Assess for malaria.
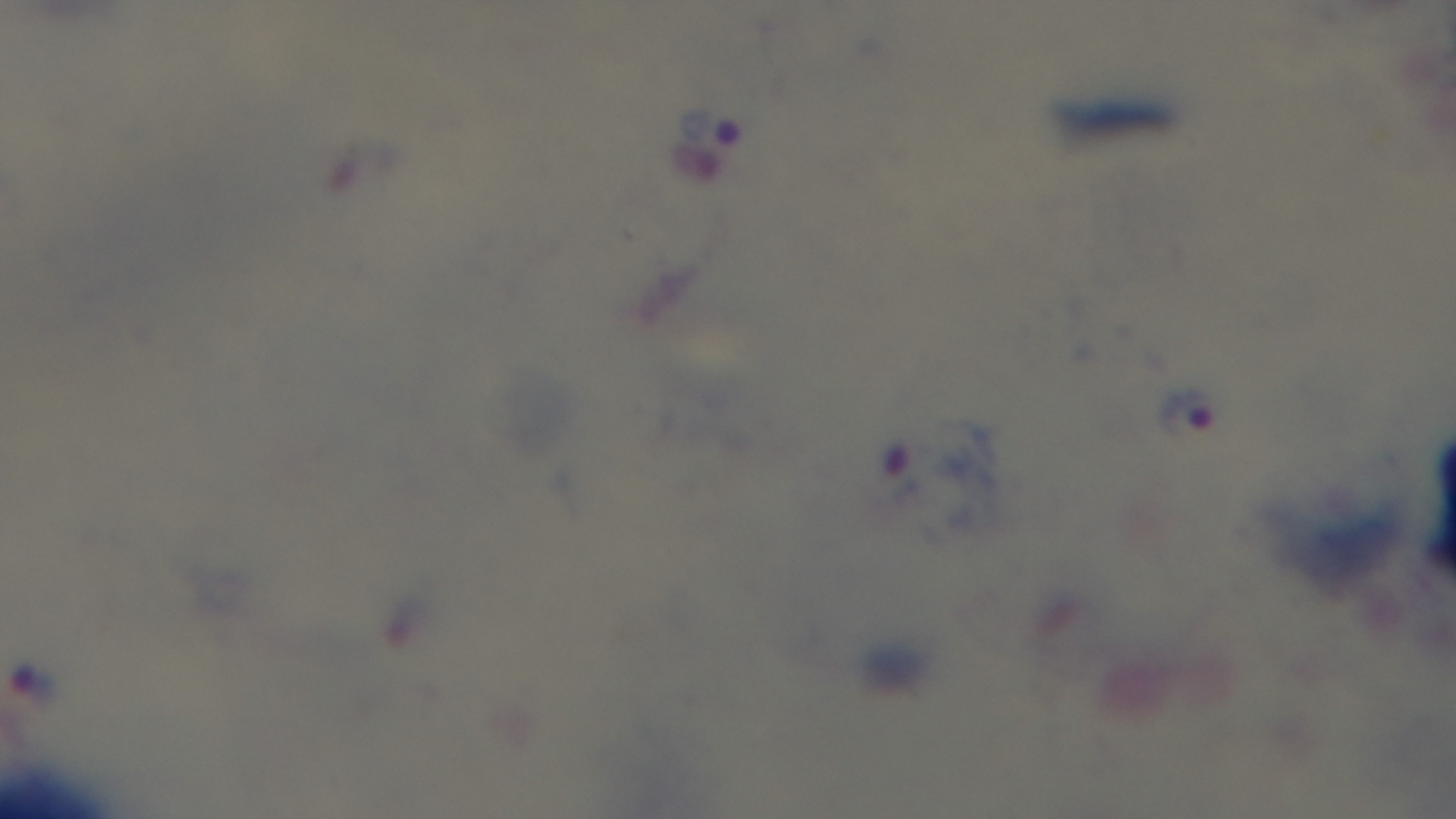
Positive.

field of view = one from the slide
preparation = thick blood film
stain = Giemsa
modality = light microscopy
objective = 100x oil immersion
capture = mounted 4K digital camera